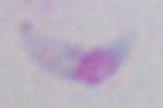

modality = micrograph
magnification = 1000x
identification = Toxoplasma gondii